Outline each blood parasite and name the species.
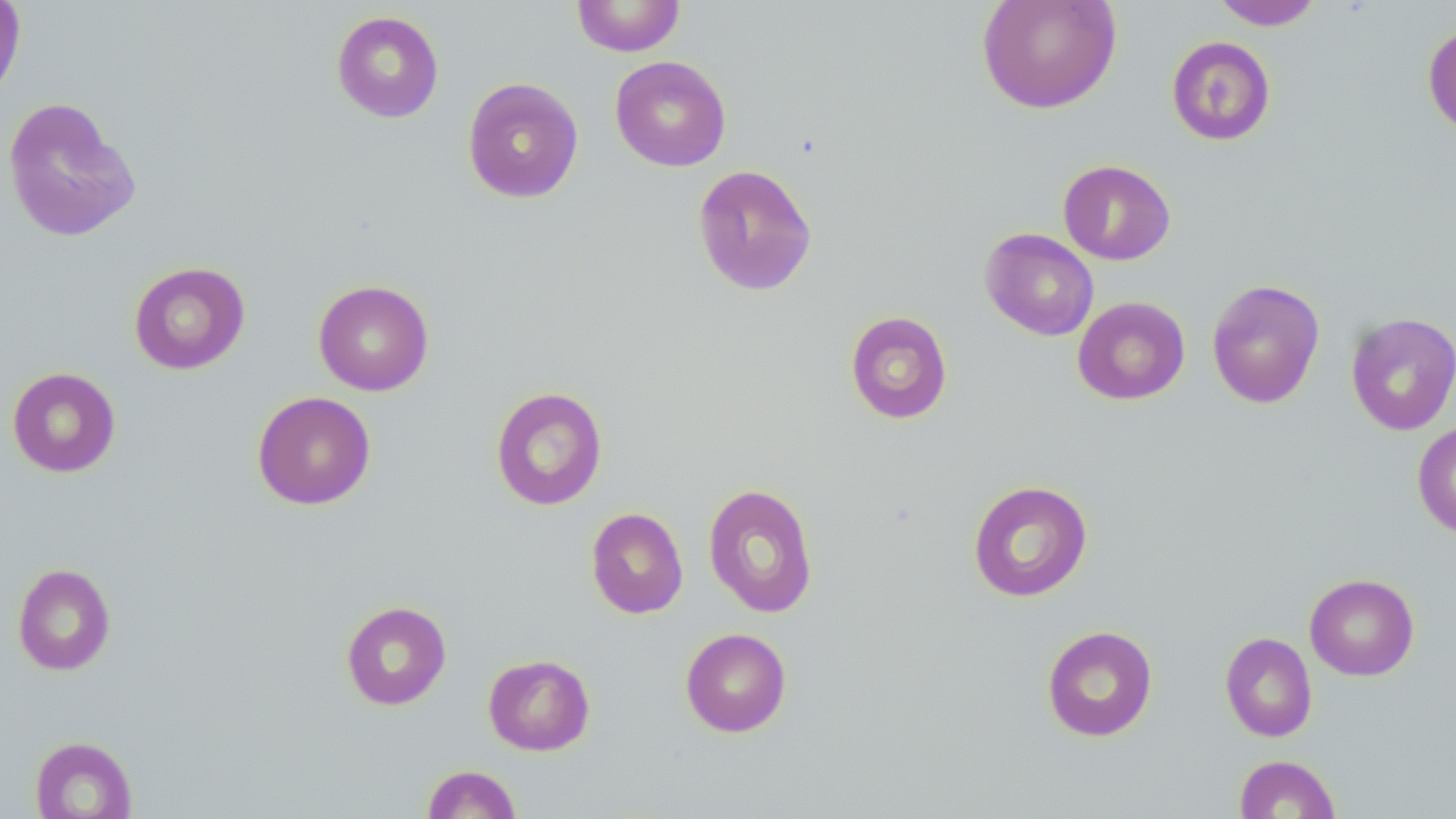
No blood parasites seen.

Approximate bounding boxes as (x1,y1)-(x2,y2) corner pairs in pixels. Uninfected red blood cell locations: (0,0)-(26,104), (571,0)-(686,57), (977,0)-(1122,115), (1210,0)-(1325,30), (331,10)-(444,123), (1423,22)-(1456,140), (1166,35)-(1276,146), (609,56)-(731,171), (462,77)-(584,203), (1,96)-(141,244), (1058,159)-(1176,265), (692,164)-(817,296), (980,228)-(1099,341), (128,261)-(251,375), (313,279)-(434,396), (1206,279)-(1325,409), (1072,296)-(1190,405), (845,311)-(952,425), (1345,313)-(1456,435), (7,367)-(121,478), (490,386)-(607,510), (252,391)-(376,510), (1412,421)-(1456,538), (967,479)-(1093,602), (702,483)-(818,618), (586,507)-(688,618), (12,563)-(116,675), (1304,573)-(1419,680), (340,600)-(452,710), (1041,625)-(1158,742), (680,627)-(792,737), (1220,632)-(1317,742), (482,653)-(595,756), (30,735)-(137,818), (1234,754)-(1341,818), (422,764)-(522,818). Slide-level diagnosis: no evidence of blood parasites. Image is 1456×819 pixels. 1000x magnification. One field of a larger specimen. Optical microscopy. May-Grünwald-Giemsa stain. Thin blood film.